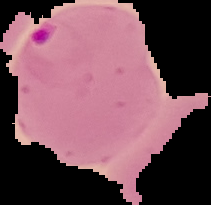

Summary:
  - Image size: 211×205 pixels
  - Preparation: thin blood smear
  - Image type: cell region segmented out of the field of view; surrounding area masked to black
  - Malaria status: parasitized